Locate every Plasmodium vivax-infected red blood cell.
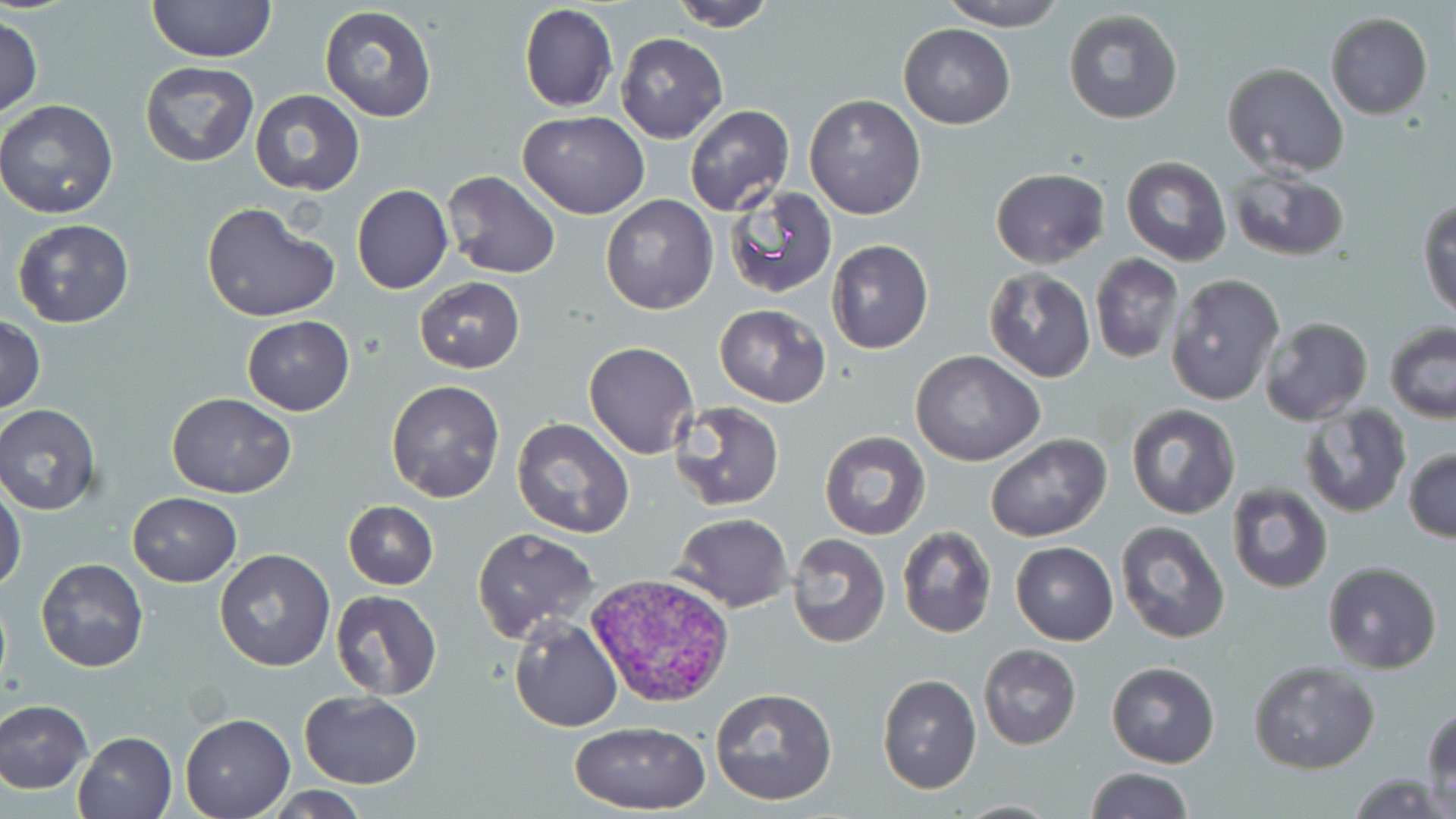
Approximate bounding boxes as [x1, y1, x2, y2] in pixels.
Plasmodium vivax-infected red blood cells: [586, 572, 734, 709].

Summary:
  - Uninfected red blood cell locations: [147, 0, 276, 65], [666, 0, 780, 30], [939, 0, 1070, 31], [518, 3, 618, 113], [317, 5, 441, 122], [1062, 9, 1184, 125], [1325, 13, 1433, 119], [0, 17, 44, 119], [898, 24, 1016, 129], [614, 31, 729, 143], [139, 61, 259, 166], [1222, 63, 1349, 178], [248, 89, 365, 196], [804, 94, 927, 220], [1, 99, 119, 219], [683, 104, 794, 216], [518, 111, 650, 218], [1121, 157, 1231, 266], [990, 167, 1110, 267], [1226, 169, 1349, 262], [443, 171, 561, 278], [351, 183, 453, 295], [724, 184, 838, 299], [600, 194, 719, 315], [1419, 196, 1456, 320], [200, 201, 338, 323], [11, 219, 136, 329], [826, 239, 934, 354], [1091, 253, 1183, 364], [982, 268, 1096, 384], [1167, 273, 1284, 406], [415, 276, 524, 373], [714, 303, 830, 406], [242, 315, 355, 416], [1, 316, 45, 412], [1259, 316, 1373, 426], [1384, 322, 1455, 424], [584, 340, 700, 459], [911, 349, 1043, 466], [385, 380, 506, 502], [166, 393, 296, 497], [667, 402, 785, 512], [1127, 402, 1241, 519], [0, 404, 103, 515], [1300, 404, 1409, 517], [512, 416, 635, 537], [819, 430, 930, 541], [985, 433, 1111, 543], [1404, 447, 1456, 543], [1226, 481, 1333, 593], [0, 484, 27, 592], [128, 492, 242, 586], [342, 500, 439, 590], [671, 512, 795, 613], [1116, 521, 1230, 643], [898, 526, 998, 640], [471, 527, 597, 644], [787, 533, 891, 649], [1010, 542, 1119, 645], [214, 547, 335, 672], [36, 558, 149, 672], [1321, 560, 1443, 674], [329, 590, 443, 700], [510, 614, 623, 731], [978, 644, 1081, 750], [1248, 660, 1380, 774], [1105, 661, 1221, 767], [877, 674, 981, 794], [709, 686, 840, 808], [298, 690, 423, 787], [0, 699, 94, 793], [1423, 705, 1455, 810], [181, 714, 294, 818], [568, 722, 712, 815], [74, 730, 178, 819], [1084, 767, 1194, 819], [1352, 772, 1449, 817], [266, 786, 374, 819], [953, 800, 1065, 817]
  - Slide-level diagnosis: Plasmodium vivax
  - Stain: May-Grünwald-Giemsa
  - Field of view: one of a larger specimen
  - Magnification: 1000x
  - Modality: optical microscopy
  - Image size: 1456×819 pixels
  - Preparation: thin blood smear